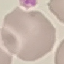

Malaria status: uninfected. Photographed with a smartphone camera at the microscope eyepiece. Cell patch, automatically extracted from a larger field of view and resized to 64 × 64 pixels. Giemsa stain. Thin blood smear.